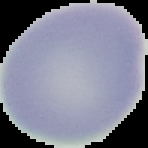

Summary:
  - Preparation: thin blood smear
  - Result: no Plasmodium parasites seen
  - Image size: 148×148 pixels
  - Image type: segmented cell region with the area outside set to black